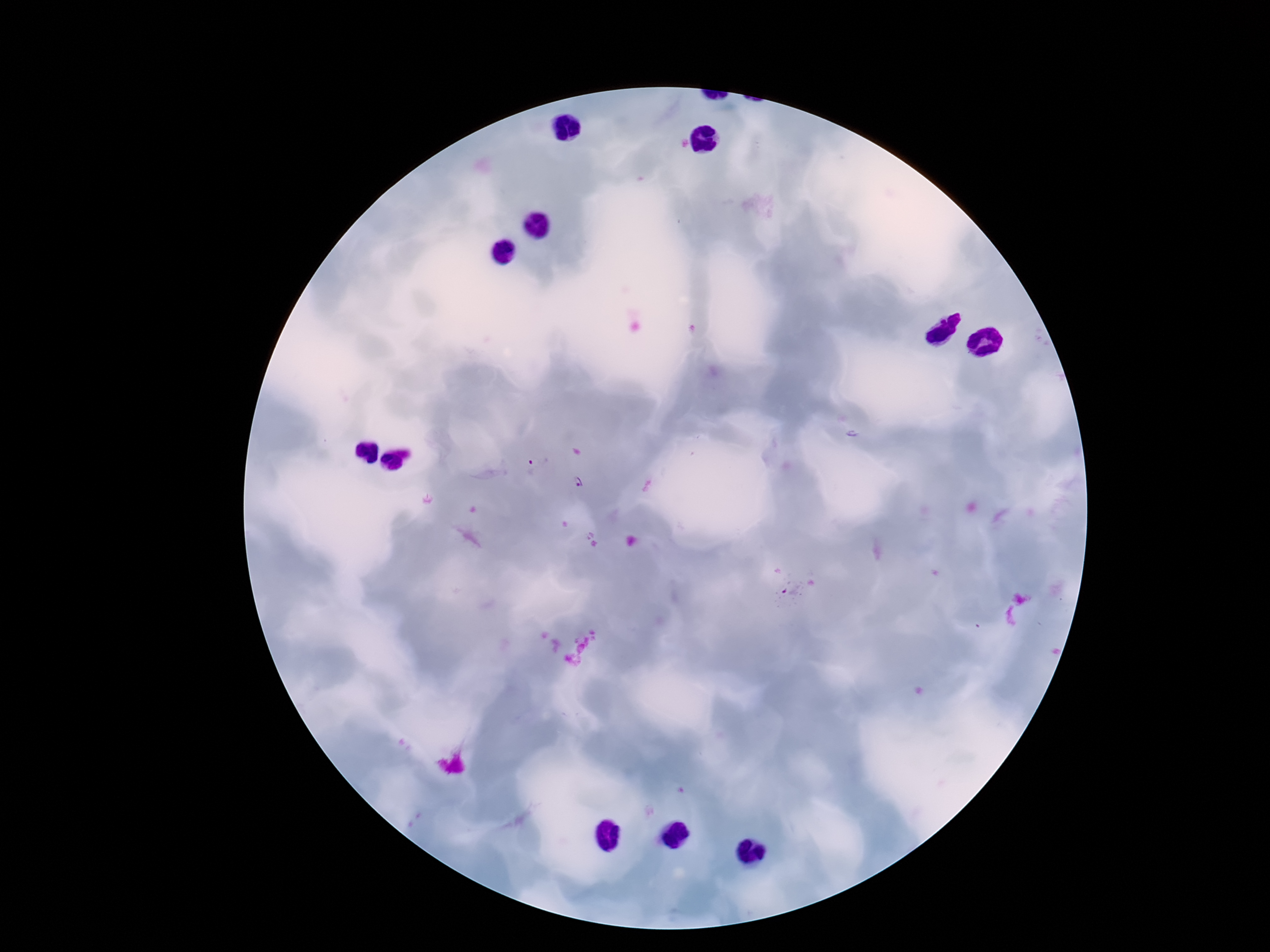

patient malaria status = infected
image size = 1270×952 pixels
field of view = one from this slide
Plasmodium parasite locations = approximate centers as {x, y} in pixels: {530, 468}, {581, 484}, {792, 591}
preparation = thick blood smear
capture = smartphone camera through the microscope eyepiece
magnification = 100x
stain = Giemsa